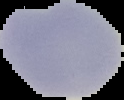

Result: negative for Plasmodium parasites. Cell region segmented out of the field of view; the surrounding area is masked to black. Image is 124×100 pixels. From a thin blood film.